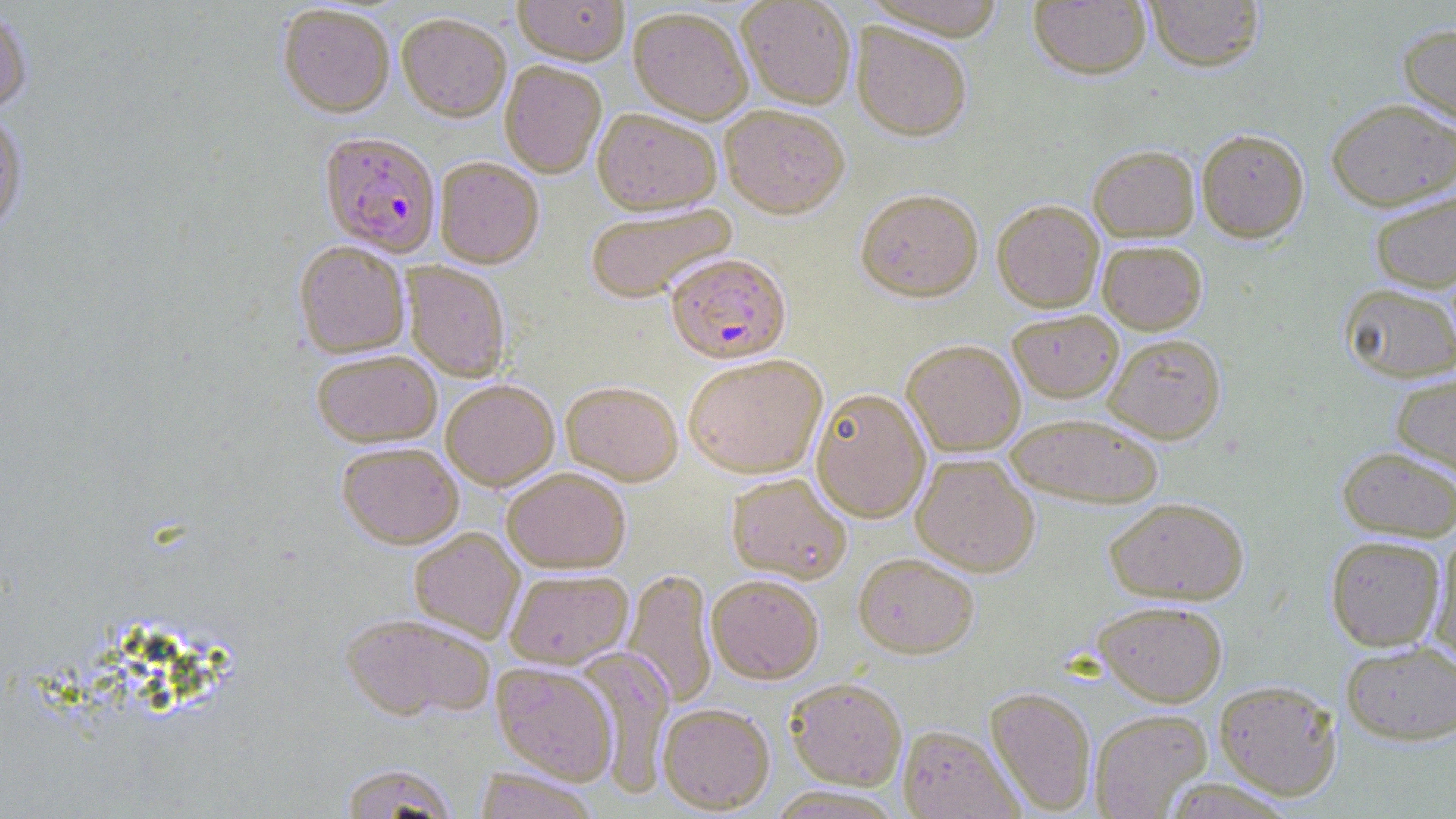

Approximate bounding boxes as (x1,y1)-(x2,y2) corner pairs in pixels. Plasmodium falciparum-infected red blood cell locations: (316,132)-(437,257), (666,252)-(791,363). Uninfected red blood cell locations: (513,0)-(629,64), (738,0)-(856,109), (865,0)-(1009,39), (1028,0)-(1151,79), (1144,0)-(1266,72), (278,4)-(395,117), (0,7)-(33,114), (628,7)-(753,123), (396,12)-(511,122), (852,22)-(972,140), (1397,22)-(1456,132), (500,61)-(606,178), (1325,98)-(1456,211), (719,104)-(849,218), (592,107)-(722,214), (0,110)-(29,234), (1197,128)-(1309,242), (1088,144)-(1199,241), (434,157)-(544,268), (855,188)-(984,302), (1369,191)-(1456,293), (992,199)-(1104,312), (585,203)-(737,304), (294,240)-(410,358), (1098,240)-(1207,333), (403,262)-(510,381), (1339,282)-(1456,383), (1007,310)-(1123,402), (1103,333)-(1226,443), (902,339)-(1026,456), (311,349)-(442,447), (325,349)-(448,547), (683,353)-(827,478), (1390,372)-(1456,479), (441,379)-(559,489), (561,380)-(683,485), (810,388)-(930,522), (1005,411)-(1165,508), (337,442)-(463,548), (1337,446)-(1455,542), (911,453)-(1040,576), (502,467)-(630,573), (726,472)-(851,583), (1105,496)-(1249,605), (409,527)-(524,642), (1325,535)-(1445,651), (1427,536)-(1456,670), (854,551)-(979,657), (624,568)-(717,708), (504,569)-(633,668), (706,574)-(824,683), (1094,600)-(1228,706), (341,612)-(494,720), (1341,640)-(1456,745), (575,649)-(676,793), (492,662)-(618,784), (786,677)-(907,790), (1213,679)-(1343,800), (985,687)-(1097,814), (658,703)-(775,813), (1090,708)-(1212,819), (898,725)-(1021,819), (338,763)-(459,818), (474,769)-(600,819). Slide-level diagnosis: Plasmodium falciparum. Captured at 1000x magnification. Thin blood film. May-Grünwald-Giemsa-stained preparation. Optical microscopy. Image is 1456×819 pixels. Single field of view.